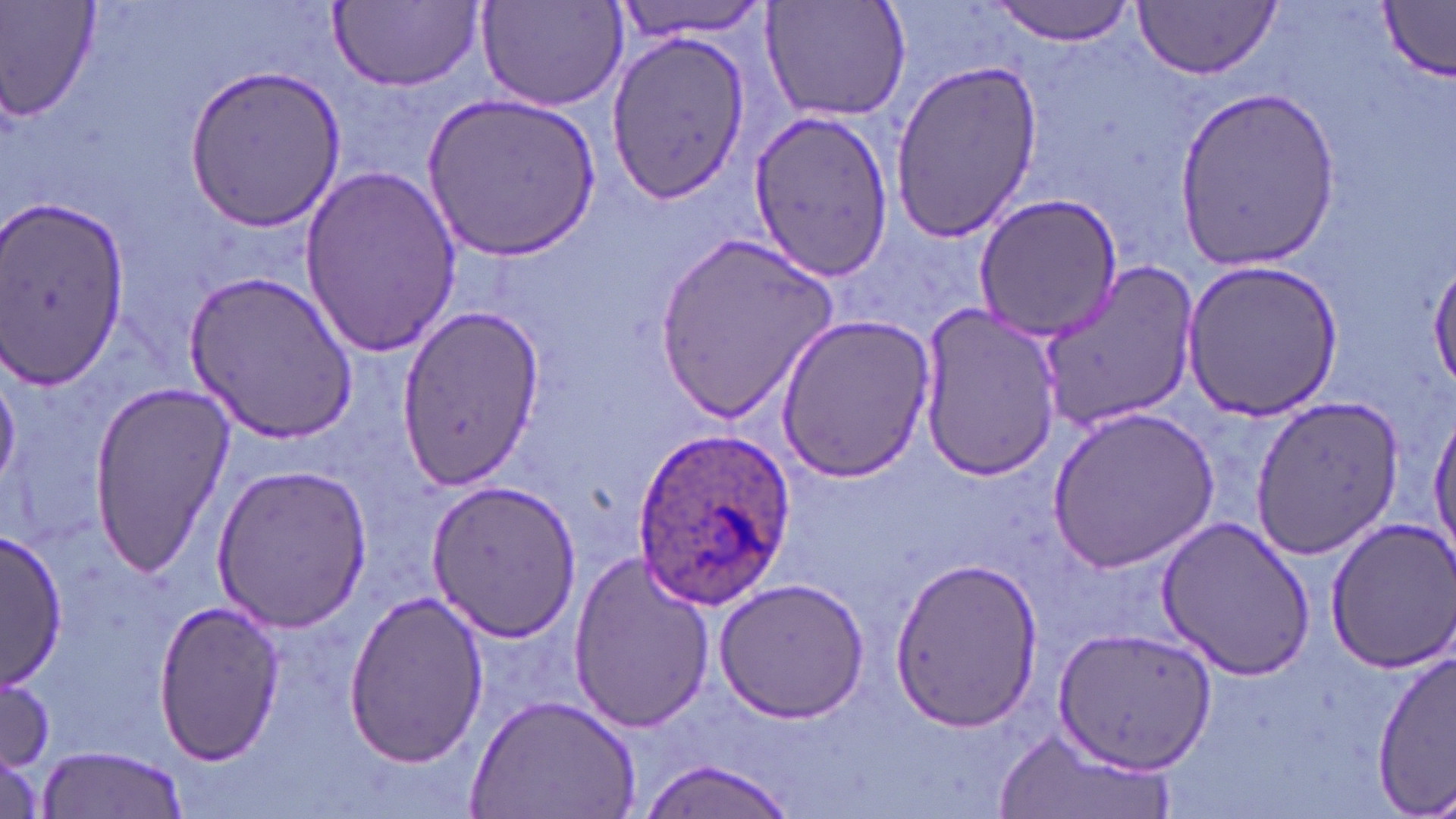
Approximate bounding boxes as [x1, y1, x2, y2] in pixels. Uninfected red blood cell locations: [0, 0, 101, 122], [476, 0, 630, 113], [607, 0, 776, 40], [762, 0, 913, 124], [989, 0, 1142, 45], [1133, 1, 1281, 79], [330, 2, 480, 92], [1378, 3, 1454, 82], [604, 34, 753, 202], [889, 58, 1044, 243], [184, 65, 344, 232], [1176, 86, 1341, 270], [424, 91, 600, 263], [745, 105, 893, 284], [297, 164, 459, 356], [973, 193, 1124, 342], [0, 197, 131, 396], [655, 231, 841, 422], [1430, 254, 1456, 397], [1181, 257, 1345, 421], [1034, 261, 1202, 432], [186, 270, 357, 443], [915, 304, 1064, 483], [392, 308, 544, 489], [775, 314, 935, 483], [86, 379, 235, 574], [1248, 394, 1405, 559], [1046, 405, 1221, 571], [1429, 406, 1456, 568], [211, 464, 371, 631], [425, 480, 580, 641], [1154, 516, 1315, 680], [1323, 517, 1456, 673], [1, 530, 66, 690], [567, 550, 717, 734], [889, 556, 1044, 734], [715, 577, 873, 722], [340, 590, 488, 769], [151, 597, 284, 768], [1051, 624, 1221, 775], [1370, 649, 1454, 813], [0, 670, 55, 776], [468, 693, 641, 818], [991, 723, 1175, 819], [34, 746, 189, 819], [634, 759, 799, 819]. Plasmodium ovale-infected red blood cell locations: [629, 426, 798, 611]. Slide-level diagnosis: Plasmodium ovale. One field of a larger specimen. Image is 1456×819 pixels. May-Grünwald-Giemsa stain. Captured at 1000x magnification. Optical microscopy. Thin blood film.